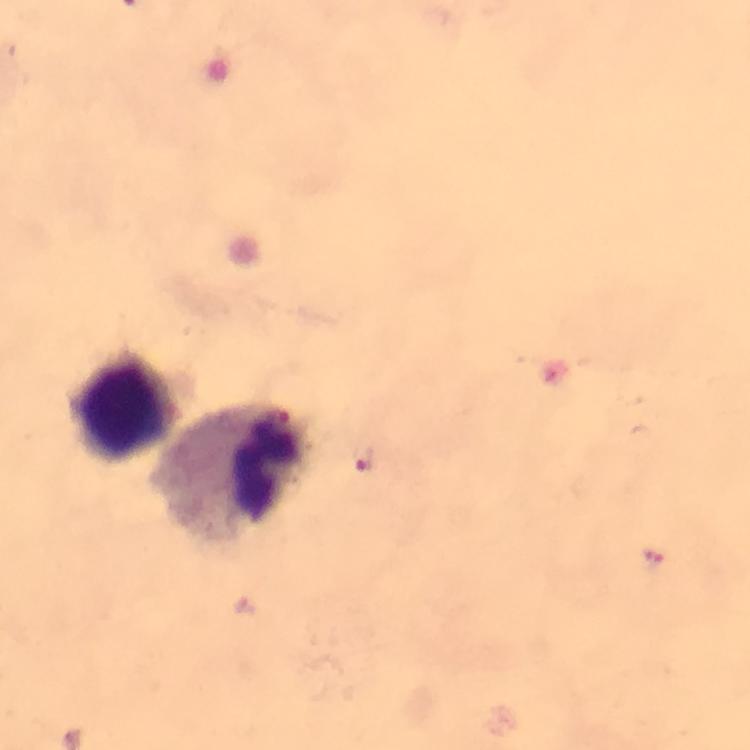
image_size: 750×750 pixels
magnification: 100x
capture: smartphone camera through the microscope
plasmodium_parasite_locations: 'approximate centers as (x, y) in pixels: (283, 421), (365, 457), (654, 560)'
cropped_from: one field of view
preparation: thick blood smear
leukocyte_locations: 'approximate centers as (x, y) in pixels: (124, 408), (234, 473)'
stain: Giemsa
immersion_oil: applied
context: from a diagnostic examination for malaria